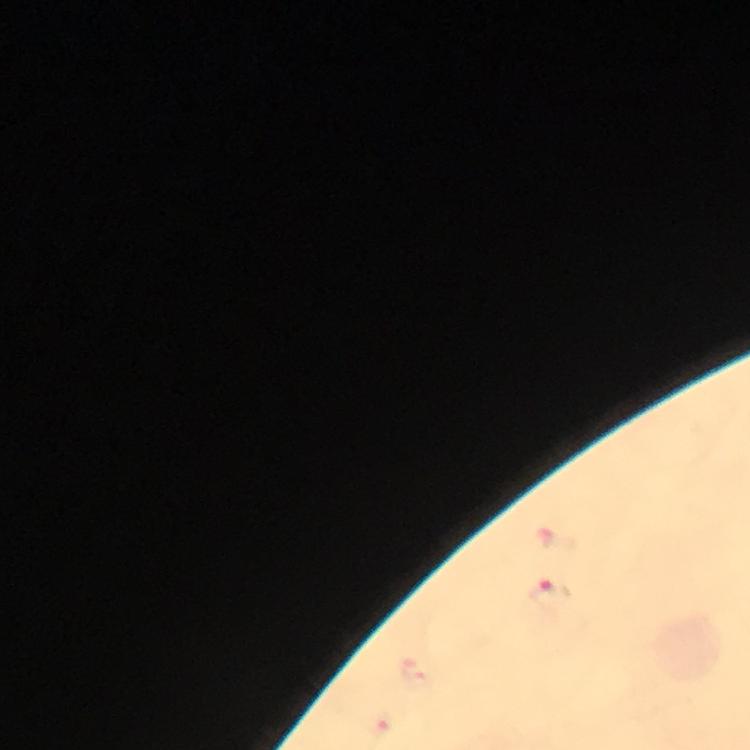
Approximate centers as [x, y] in pixels.
Summary:
  - Malaria parasite locations: [550, 594]
  - Stain: Giemsa
  - Immersion oil: used
  - Context: from a malaria diagnostic workup
  - Image size: 750×750 pixels
  - Magnification: 100x
  - Capture: smartphone camera through the microscope
  - Preparation: thick blood smear
  - Cropped from: a single field of view